Outline every leukocyte.
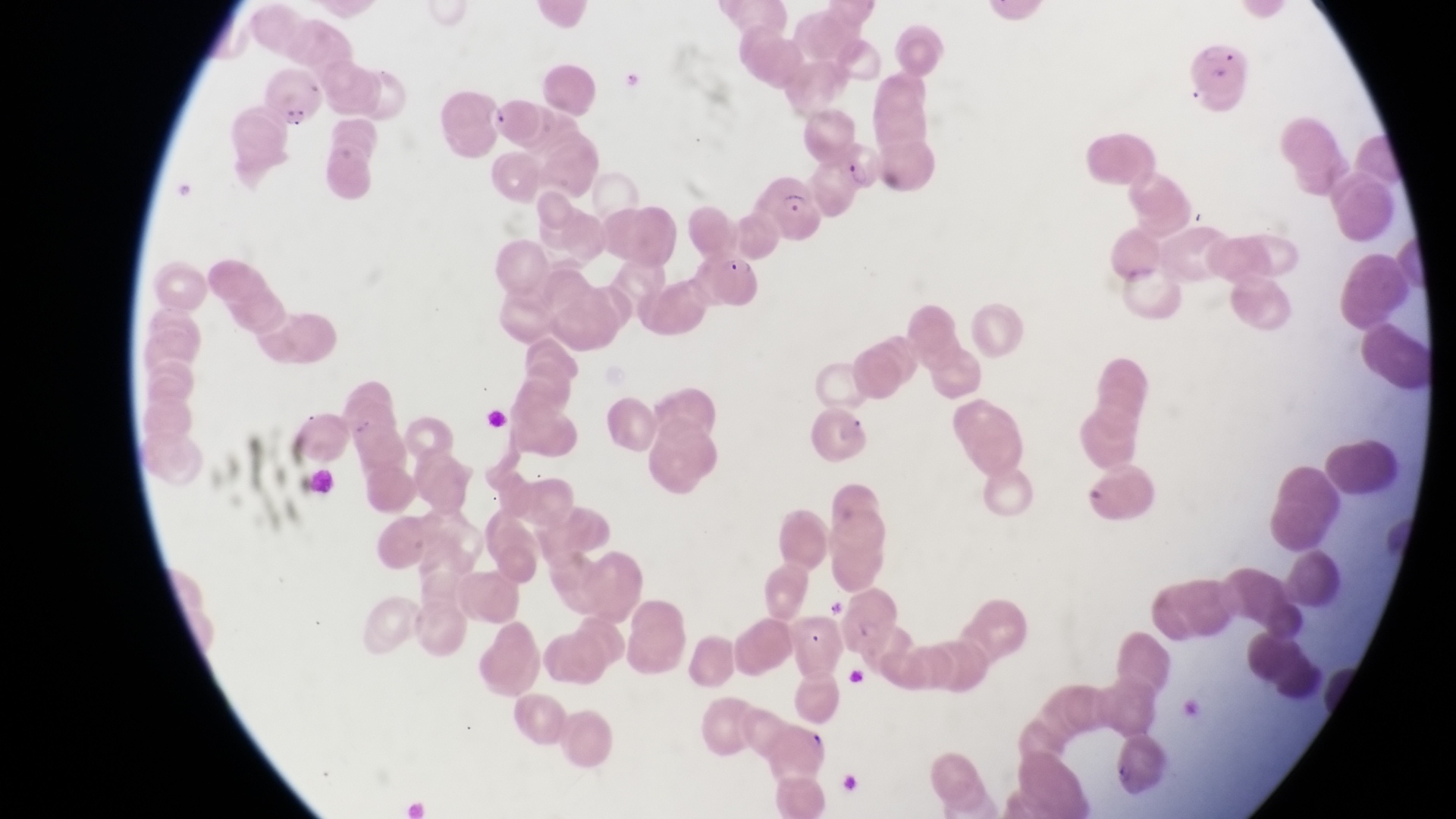

No leukocytes observed.

preparation: thin blood smear
magnification: 1000x
parasitised_red_blood_cell_locations: 'approximate bounding boxes as {left, top, right, bottom} in pixels: {1191, 45, 1250, 114}, {482, 95, 545, 142}, {832, 138, 888, 198}, {766, 177, 825, 241}, {698, 240, 757, 311}'
capture: smartphone photograph through the eyepiece of an Olympus CX-23 microscope
image_size: 1456×819 pixels
country: Uganda
field_of_view: single